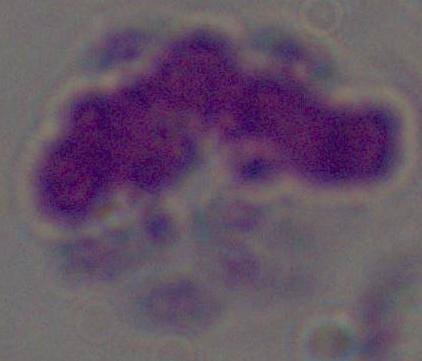 Micrograph. A leukocyte is seen. Captured at 1000x magnification.